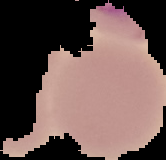
image size = 166×160 pixels
image type = segmented cell region on a black background
malaria status = uninfected
preparation = thin blood smear